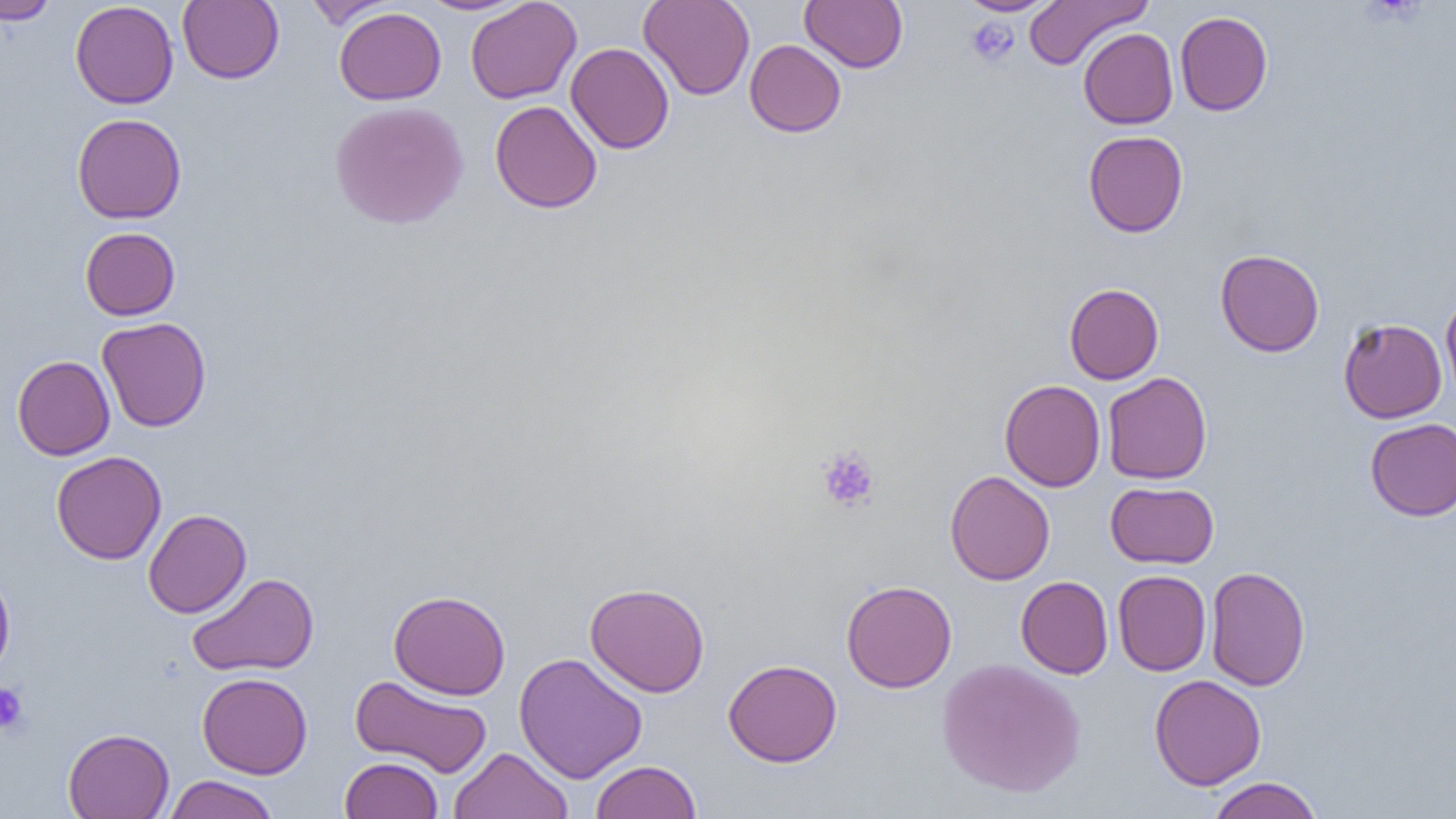
Summary:
  - Coordinate format: approximate bounding boxes as named x1/y1/x2/y2 corners in pixels
  - Uninfected red blood cell locations: (x1=178, y1=0, x2=284, y2=84), (x1=417, y1=0, x2=533, y2=15), (x1=465, y1=0, x2=582, y2=104), (x1=638, y1=0, x2=755, y2=100), (x1=800, y1=0, x2=908, y2=72), (x1=958, y1=0, x2=1060, y2=16), (x1=1024, y1=0, x2=1151, y2=70), (x1=0, y1=1, x2=58, y2=25), (x1=70, y1=1, x2=179, y2=109), (x1=303, y1=1, x2=396, y2=29), (x1=334, y1=7, x2=446, y2=105), (x1=1175, y1=11, x2=1273, y2=116), (x1=1078, y1=28, x2=1178, y2=129), (x1=745, y1=39, x2=846, y2=137), (x1=565, y1=43, x2=674, y2=153), (x1=329, y1=100, x2=469, y2=230), (x1=489, y1=100, x2=602, y2=214), (x1=72, y1=113, x2=187, y2=224), (x1=1083, y1=130, x2=1188, y2=237), (x1=80, y1=227, x2=180, y2=320), (x1=1215, y1=249, x2=1324, y2=357), (x1=1064, y1=283, x2=1164, y2=384), (x1=1440, y1=292, x2=1456, y2=403), (x1=97, y1=317, x2=211, y2=432), (x1=1338, y1=318, x2=1447, y2=423), (x1=12, y1=355, x2=115, y2=460), (x1=1102, y1=372, x2=1212, y2=484), (x1=999, y1=379, x2=1106, y2=492), (x1=1365, y1=418, x2=1456, y2=521), (x1=51, y1=450, x2=166, y2=564), (x1=945, y1=470, x2=1055, y2=585), (x1=1106, y1=481, x2=1219, y2=568), (x1=143, y1=509, x2=252, y2=618), (x1=0, y1=566, x2=16, y2=683), (x1=1205, y1=566, x2=1311, y2=691), (x1=1113, y1=570, x2=1211, y2=676), (x1=187, y1=572, x2=319, y2=677), (x1=1015, y1=576, x2=1113, y2=679), (x1=841, y1=580, x2=957, y2=693), (x1=585, y1=582, x2=710, y2=697), (x1=388, y1=590, x2=511, y2=699), (x1=514, y1=652, x2=647, y2=783), (x1=723, y1=658, x2=842, y2=767), (x1=937, y1=658, x2=1086, y2=799), (x1=197, y1=672, x2=312, y2=779), (x1=350, y1=674, x2=494, y2=778), (x1=1150, y1=674, x2=1266, y2=790), (x1=63, y1=728, x2=174, y2=819), (x1=449, y1=747, x2=574, y2=818), (x1=340, y1=756, x2=443, y2=818), (x1=590, y1=760, x2=702, y2=819), (x1=165, y1=774, x2=278, y2=818), (x1=1208, y1=777, x2=1322, y2=819)
  - Platelet locations: (x1=965, y1=17, x2=1019, y2=68), (x1=816, y1=446, x2=879, y2=512), (x1=0, y1=683, x2=29, y2=735)
  - Slide-level diagnosis: negative for blood parasites
  - Image size: 1456×819 pixels
  - Magnification: 1000x
  - Field of view: single
  - Modality: light microscopy
  - Preparation: thin blood film